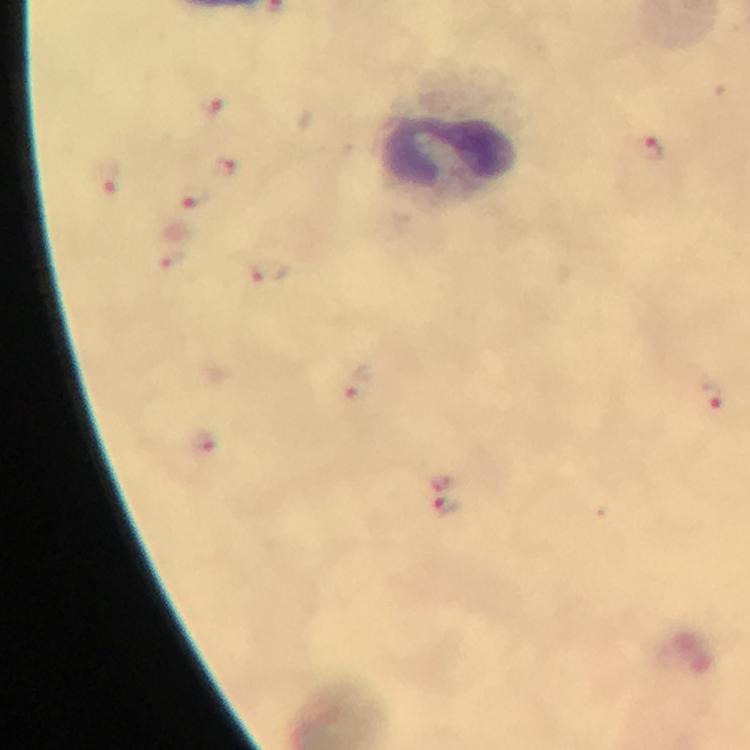
cropped from = one field of view
image size = 750×750 pixels
leukocyte locations = approximate centers as {x, y} in pixels: {455, 133}
immersion oil = applied
context = from a diagnostic examination for malaria
capture = smartphone photograph through a microscope
stain = Giemsa
magnification = 100x
malaria parasite locations = approximate centers as {x, y} in pixels: {207, 104}, {650, 148}, {224, 167}, {107, 179}, {194, 196}, {174, 260}, {270, 269}, {358, 382}, {710, 394}, {203, 442}, {445, 483}, {446, 506}
preparation = thick blood smear